Locate every Plasmodium parasite and every leukocyte.
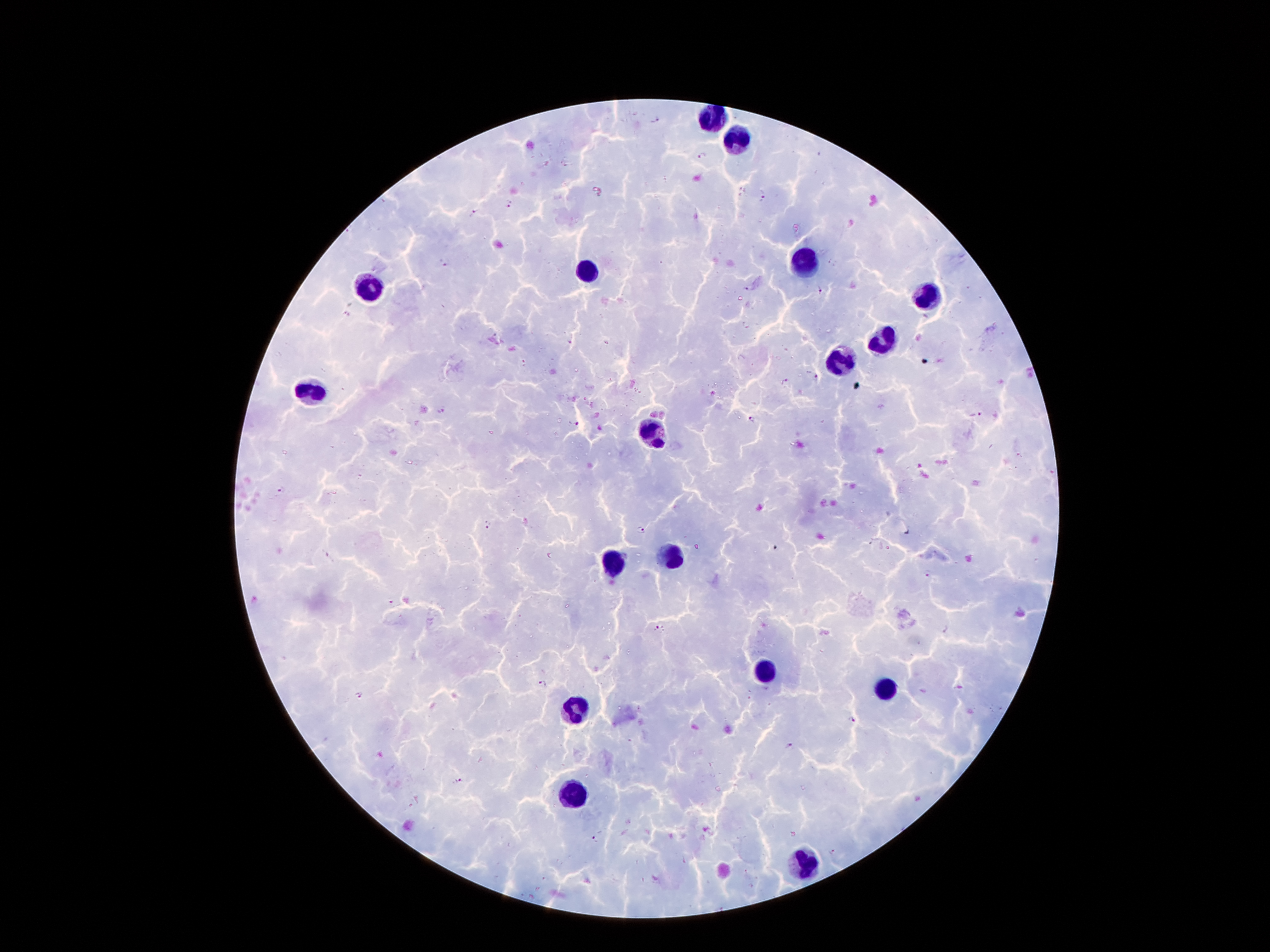
Approximate centers as {x, y} in pixels.
Plasmodium parasites: {656, 120}, {703, 157}, {764, 197}, {510, 205}, {475, 213}, {443, 263}, {745, 289}, {821, 291}, {817, 379}, {785, 381}, {441, 411}, {976, 415}, {753, 419}, {577, 424}, {281, 490}, {487, 526}, {641, 529}, {328, 556}, {927, 574}, {391, 604}, {660, 628}, {946, 629}, {542, 684}, {360, 695}, {852, 720}, {789, 746}, {460, 781}, {593, 839}, {831, 852}.
Leukocytes: {710, 117}, {737, 142}, {802, 260}, {586, 272}, {365, 289}, {926, 295}, {880, 341}, {840, 362}, {311, 398}, {655, 434}, {674, 556}, {615, 564}, {767, 673}, {886, 690}, {571, 709}, {571, 797}, {800, 862}.

Summary:
  - Preparation: thick blood film
  - Magnification: 100x
  - Field of view: single
  - Patient malaria status: infected with Plasmodium falciparum
  - Image size: 1270×952 pixels
  - Capture: smartphone through the microscope eyepiece
  - Stain: Giemsa